Name the parasite shown.
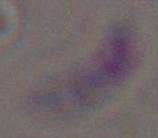
This is Toxoplasma gondii.

Captured at 1000x magnification. Photomicrograph.